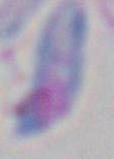

Summary:
  - Modality: micrograph
  - Magnification: 1000x
  - Identification: Toxoplasma gondii